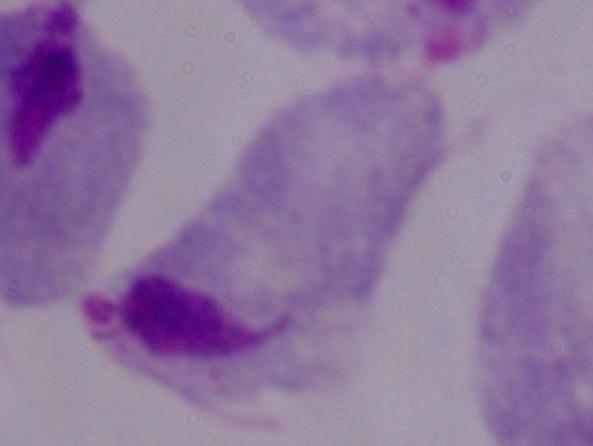
magnification: 1000x
modality: micrograph
identification: trichomonad